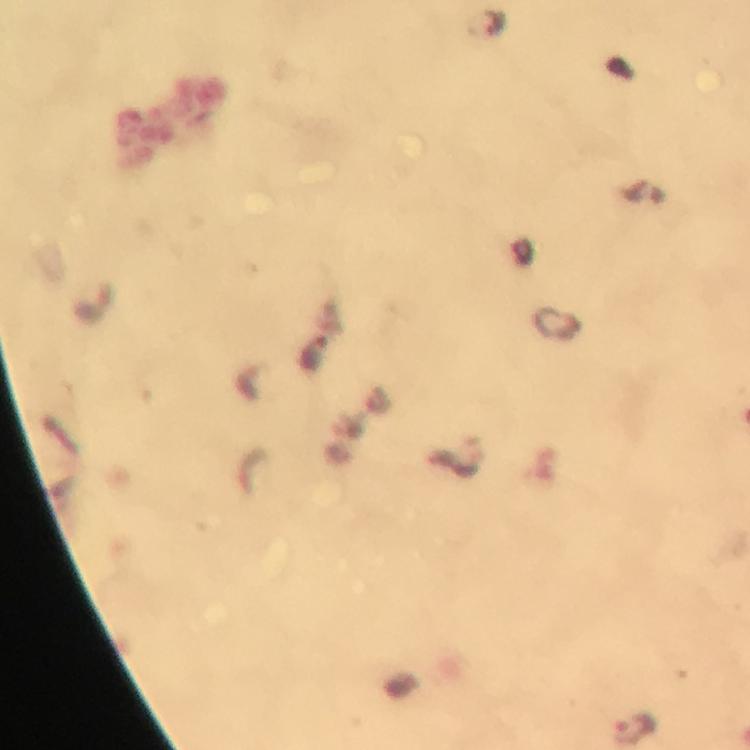

{
  "context": "from a malaria diagnostic workup",
  "preparation": "thick blood film",
  "immersion_oil": "used",
  "cropped_from": "one field of view",
  "malaria_parasite_locations": "approximate centers as (x, y) in pixels: (316, 355), (634, 728)",
  "magnification": "100x",
  "capture": "smartphone camera through the microscope",
  "stain": "Giemsa",
  "image_size": "750×750 pixels"
}